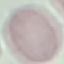 Result: no malaria parasites detected. Giemsa-stained preparation. Photographed with a smartphone camera at the microscope eyepiece. Automatically extracted cell patch, resized to 64 × 64 pixels. Thin smear of blood.